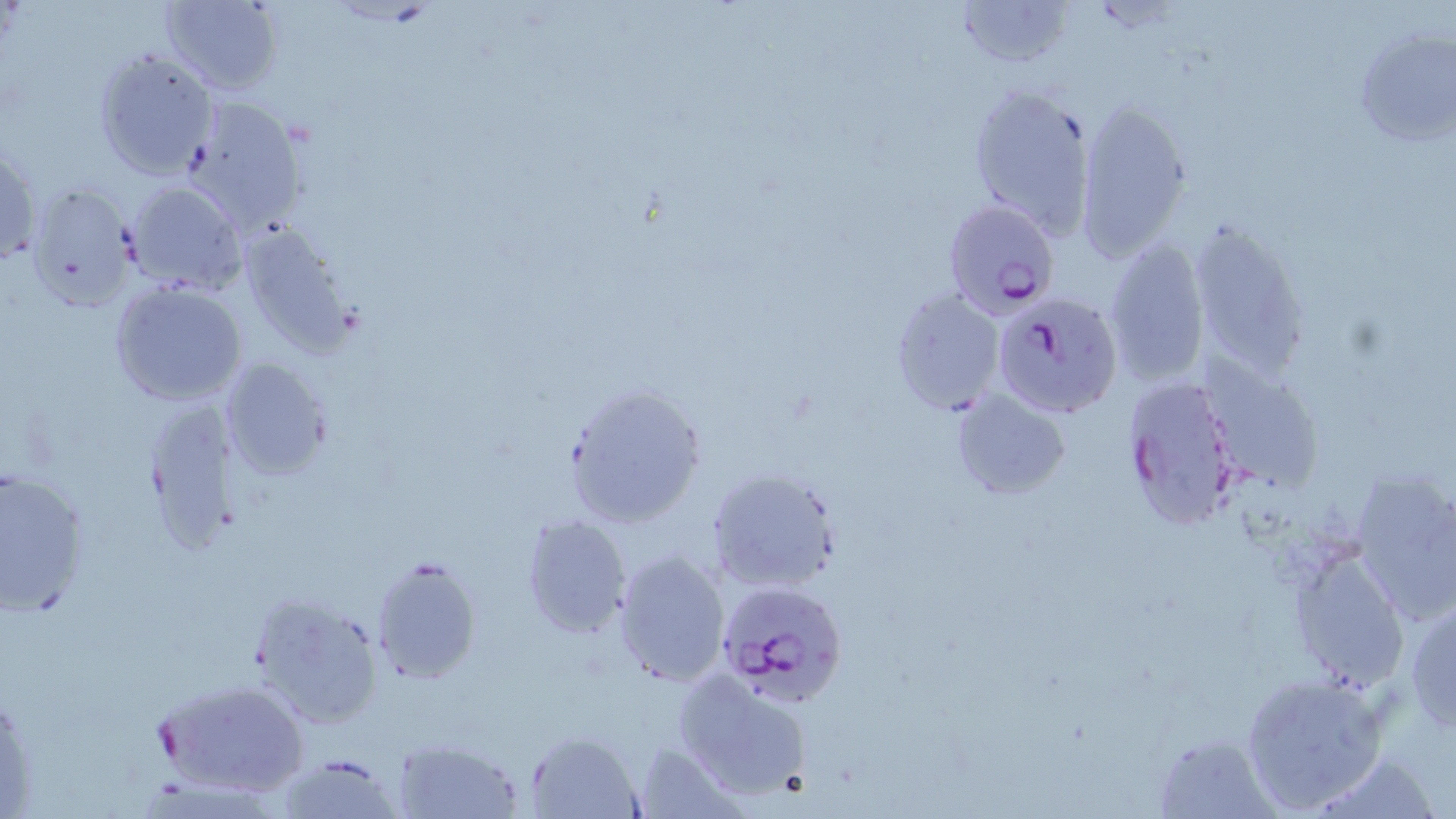
slide-level diagnosis = Plasmodium falciparum
magnification = 1000x
field of view = single
Plasmodium falciparum-infected red blood cell locations = approximate bounding boxes as (x1,y1)-(x2,y2) corner pairs in pixels: (941,201)-(1059,322), (1004,305)-(1119,428), (1118,374)-(1240,533), (716,581)-(848,708), (152,676)-(310,801)
preparation = thin blood smear
stain = May-Grünwald-Giemsa
uninfected red blood cell locations = approximate bounding boxes as (x1,y1)-(x2,y2) corner pairs in pixels: (160,0)-(284,95), (952,0)-(1076,70), (1353,28)-(1456,150), (93,47)-(218,181), (967,86)-(1094,239), (182,96)-(310,236), (1075,100)-(1194,260), (1,138)-(42,268), (127,181)-(248,295), (24,182)-(138,311), (1185,219)-(1310,377), (235,223)-(362,357), (1102,237)-(1211,386), (109,279)-(249,407), (888,287)-(1006,416), (218,357)-(335,480), (1202,360)-(1324,497), (562,382)-(708,530), (951,390)-(1071,499), (136,394)-(244,555), (0,467)-(93,617), (706,467)-(842,597), (1349,469)-(1456,624), (519,513)-(632,640), (612,550)-(731,688), (1290,550)-(1410,690), (370,555)-(482,683), (249,593)-(384,731), (1405,597)-(1456,731), (673,669)-(812,801), (1240,671)-(1392,814), (524,729)-(647,818), (1154,735)-(1277,816), (390,738)-(524,817), (630,739)-(746,818), (1307,748)-(1440,818), (274,753)-(404,818)
modality = optical microscopy
image size = 1456×819 pixels